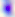
400x magnification. Micrograph. Toxoplasma gondii is shown.